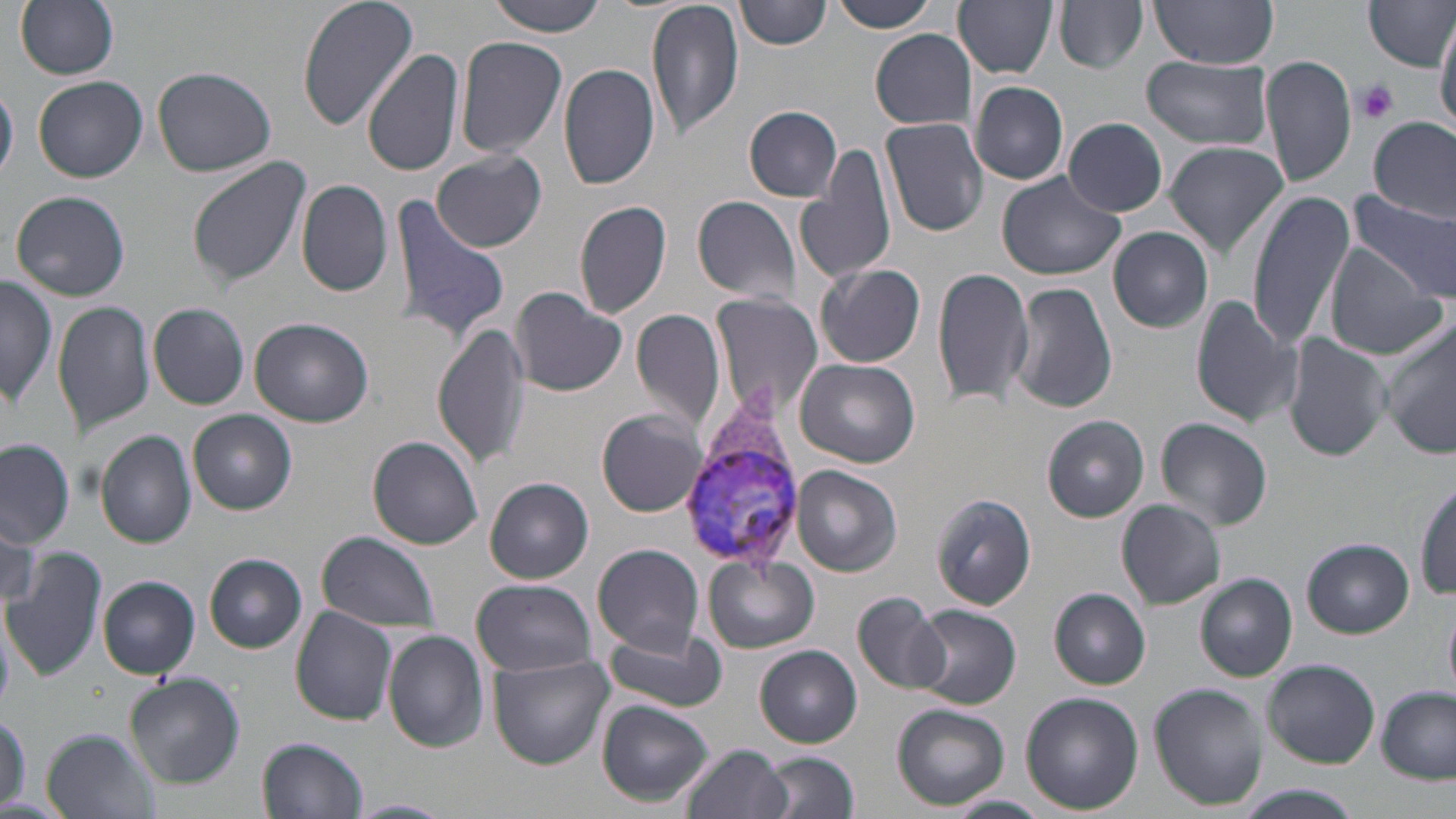
slide-level diagnosis = Plasmodium vivax
uninfected red blood cell locations = approximate bounding boxes as (x1, y1, x2, y2) in pixels: (296, 0, 419, 132), (487, 0, 611, 35), (646, 0, 743, 140), (738, 0, 829, 50), (829, 0, 939, 33), (954, 0, 1058, 77), (1055, 0, 1148, 74), (1150, 0, 1280, 68), (14, 1, 119, 79), (1363, 1, 1456, 69), (1436, 12, 1456, 131), (869, 30, 977, 130), (455, 33, 568, 160), (364, 48, 463, 177), (1259, 53, 1358, 188), (1139, 54, 1275, 150), (559, 62, 661, 192), (153, 65, 278, 176), (32, 75, 146, 182), (970, 80, 1069, 185), (0, 83, 19, 184), (744, 106, 842, 201), (1369, 115, 1454, 220), (880, 116, 988, 236), (1064, 117, 1169, 216), (1164, 142, 1289, 260), (796, 145, 900, 289), (431, 149, 546, 252), (188, 158, 310, 286), (997, 170, 1130, 283), (297, 179, 392, 297), (1247, 189, 1355, 353), (10, 190, 131, 302), (1348, 191, 1455, 301), (384, 193, 511, 342), (692, 194, 802, 306), (574, 200, 673, 320), (1108, 226, 1213, 332), (1322, 247, 1446, 357), (815, 263, 926, 368), (931, 265, 1034, 409), (1, 276, 58, 408), (1008, 282, 1116, 416), (510, 287, 628, 397), (709, 291, 824, 420), (1191, 296, 1302, 429), (53, 301, 155, 435), (149, 303, 249, 409), (632, 309, 727, 434), (249, 318, 374, 428), (433, 321, 531, 469), (1381, 325, 1456, 460), (1283, 333, 1391, 462), (794, 357, 920, 468), (598, 408, 708, 517), (189, 410, 297, 514), (1041, 415, 1150, 522), (1154, 416, 1273, 530), (95, 431, 198, 549), (368, 435, 484, 549), (0, 441, 76, 547), (792, 466, 901, 578), (486, 477, 594, 583), (1415, 482, 1455, 599), (930, 494, 1036, 610), (1115, 500, 1226, 609), (0, 516, 40, 616), (318, 532, 439, 632), (1301, 539, 1414, 637), (592, 543, 705, 655), (1, 547, 105, 681), (204, 553, 308, 653), (703, 554, 818, 653), (1195, 573, 1297, 681), (98, 575, 201, 678), (470, 580, 600, 676), (1050, 588, 1152, 688), (853, 590, 950, 696), (908, 604, 1023, 709), (290, 607, 399, 728), (1444, 607, 1456, 697), (601, 627, 728, 712), (382, 630, 489, 753), (754, 645, 863, 747), (489, 653, 614, 769), (1262, 659, 1381, 766), (123, 676, 244, 787), (1151, 685, 1269, 811), (1377, 687, 1454, 783), (1020, 691, 1144, 814), (597, 700, 713, 803), (892, 704, 1009, 810), (0, 714, 27, 806), (41, 729, 161, 818), (258, 736, 369, 818), (679, 743, 792, 819), (759, 752, 857, 819), (1241, 786, 1358, 819), (943, 795, 1051, 819), (348, 798, 454, 818)
modality = optical microscopy
platelet locations = approximate bounding boxes as (x1, y1, x2, y2) in pixels: (1355, 80, 1399, 124)
Plasmodium vivax-infected red blood cell locations = approximate bounding boxes as (x1, y1, x2, y2) in pixels: (679, 417, 805, 570)
image size = 1456×819 pixels
field of view = one of a larger specimen
stain = May-Grünwald-Giemsa
magnification = 1000x
preparation = thin blood film